Describe the morphology of the red blood cells.
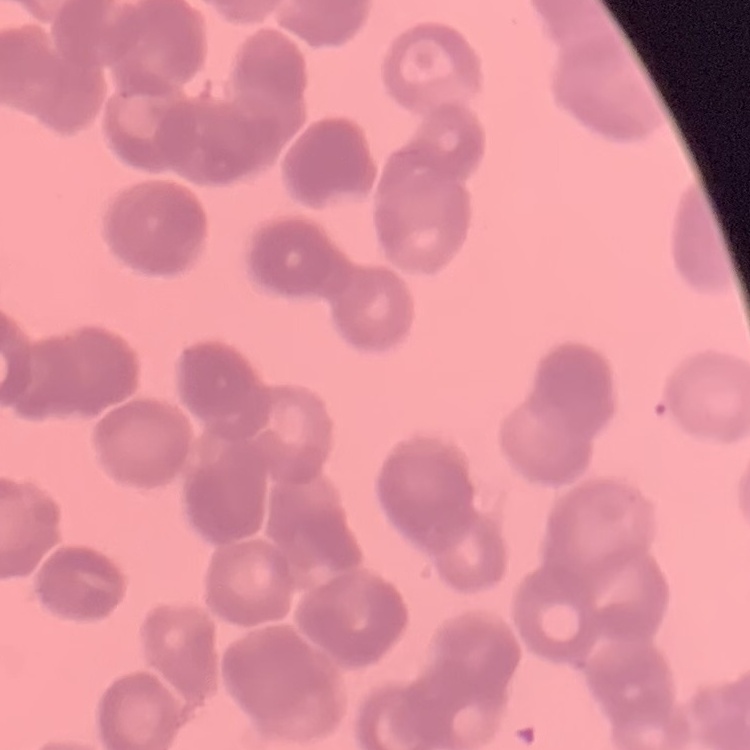

They show rouleaux formation.

Summary:
  - Image type: square crop of a larger photomicrograph
  - Preparation: thin peripheral smear
  - Stain: Field's or Giemsa